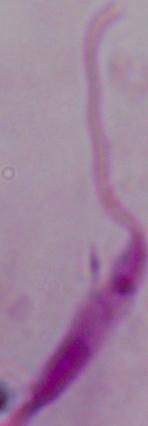
1000x magnification. A Leishmania parasite is seen. Photomicrograph.